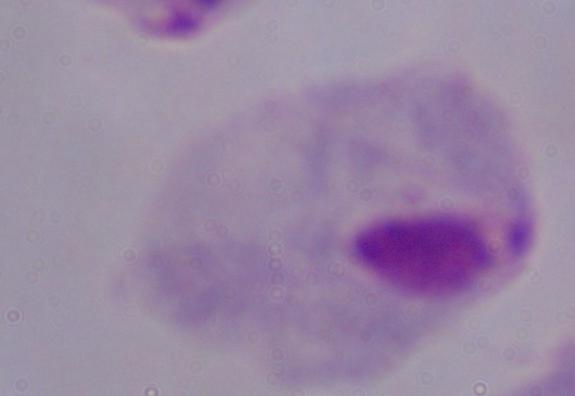
Summary:
  - Magnification: 1000x
  - Identification: trichomonad
  - Modality: photomicrograph